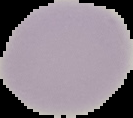

Summary:
  - Image size: 133×118 pixels
  - Image type: cell region segmented out of the field of view; surrounding area masked to black
  - Preparation: thin blood film
  - Result: negative for malaria parasites